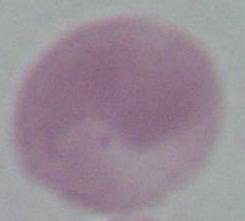
Summary:
  - Modality: micrograph
  - Identification: erythrocyte
  - Magnification: 1000x